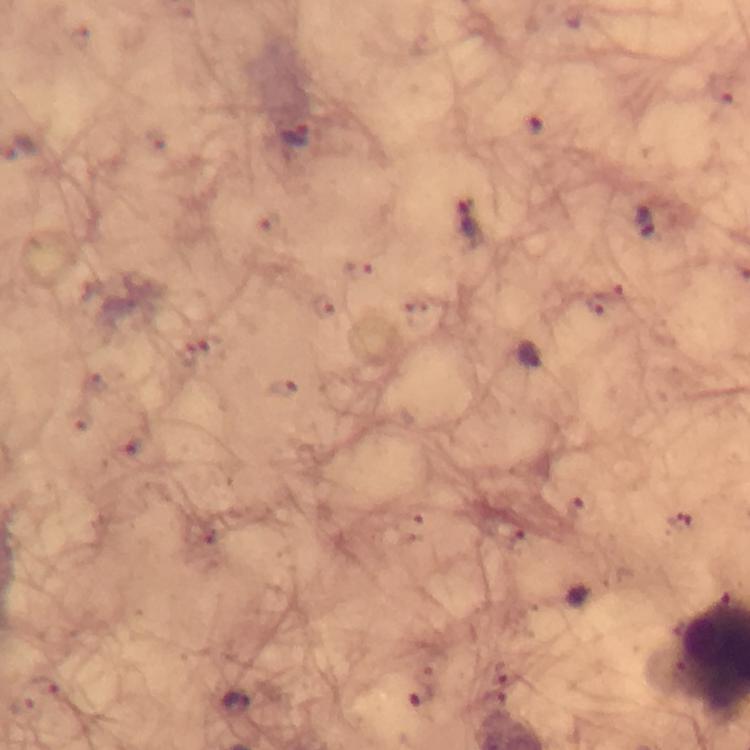
Approximate centers as (x, y) in pixels.
Summary:
  - Plasmodium parasite locations: (533, 132), (296, 134), (472, 222), (647, 222), (359, 269), (607, 301), (325, 306), (195, 352), (530, 353), (284, 387), (137, 446), (511, 532), (46, 684), (420, 692), (236, 699), (26, 710)
  - Magnification: 100x
  - Image size: 750×750 pixels
  - Stain: Giemsa
  - Cropped from: one field of view
  - Immersion oil: applied
  - Context: from a malaria diagnostic workup
  - Capture: smartphone mounted on the microscope
  - Preparation: thick blood film